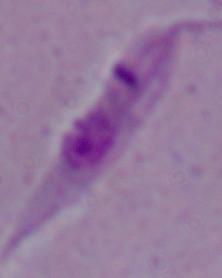 Photomicrograph. A Leishmania parasite is seen. Captured at 1000x magnification.